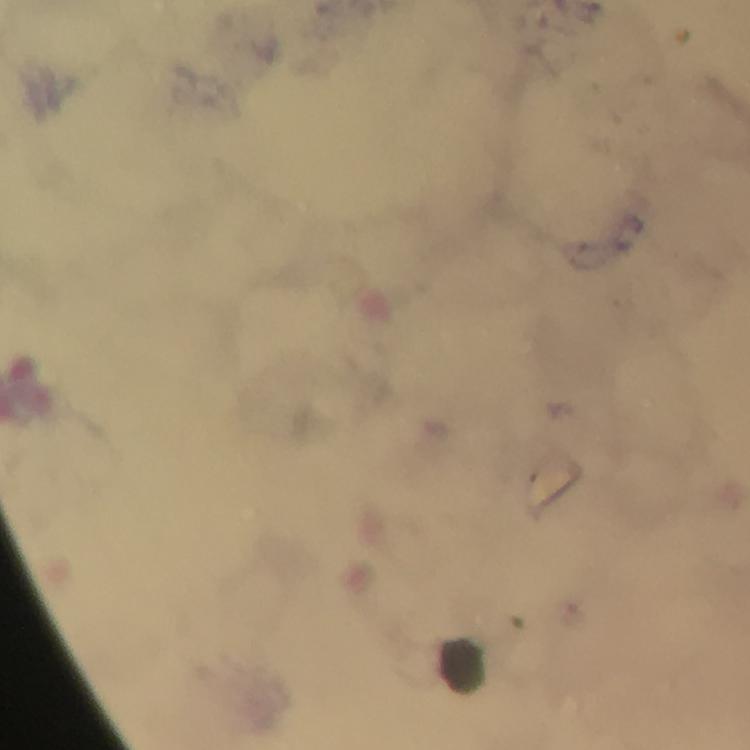

{
  "image_size": "750×750 pixels",
  "cropped_from": "one field of view",
  "plasmodium_parasites": "none seen",
  "immersion_oil": "used",
  "capture": "smartphone mounted on the microscope",
  "magnification": "100x",
  "context": "from a diagnostic examination for malaria",
  "stain": "Giemsa",
  "preparation": "thick blood film",
  "leukocyte_locations": "approximate centers as [x, y] in pixels: [463, 664]"
}